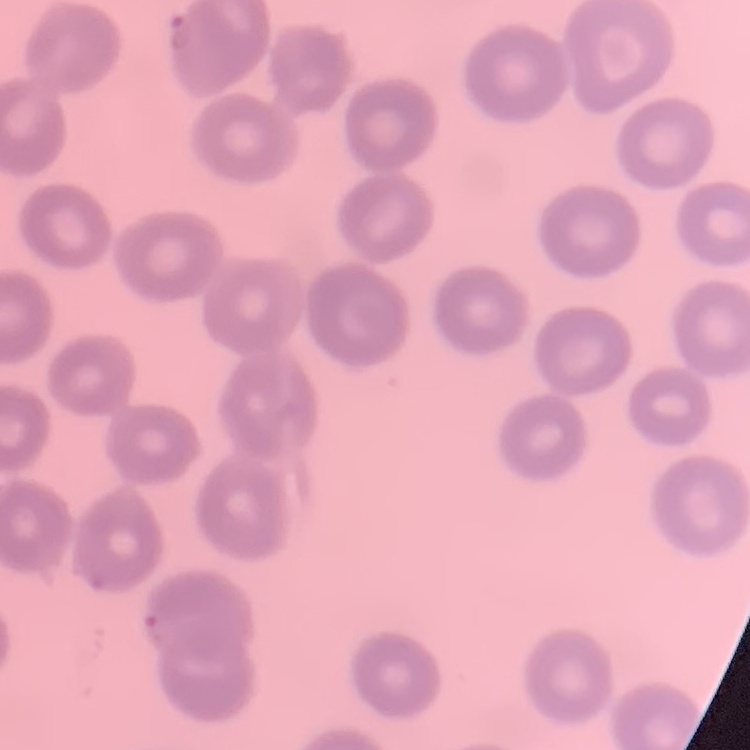

erythrocyte morphology = no rouleaux formation
preparation = thin blood smear
stain = Field's or Giemsa
image type = one tile cut from a larger photomicrograph